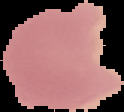
From a thin blood film. Image is 124×112 pixels. Segmented cell region on a black background. Malaria status: uninfected.